Classify this cell by malaria status.
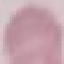
Uninfected.

Giemsa stain. Automatically extracted cell patch, resized to 64 × 64 pixels. Thin smear of blood. Photographed with a smartphone camera at the microscope eyepiece.